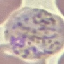

result = malaria parasites detected
capture = smartphone through the microscope eyepiece
stain = Giemsa
preparation = thin smear
image type = cell patch, automatically extracted from a larger field of view and resized to 64 × 64 pixels